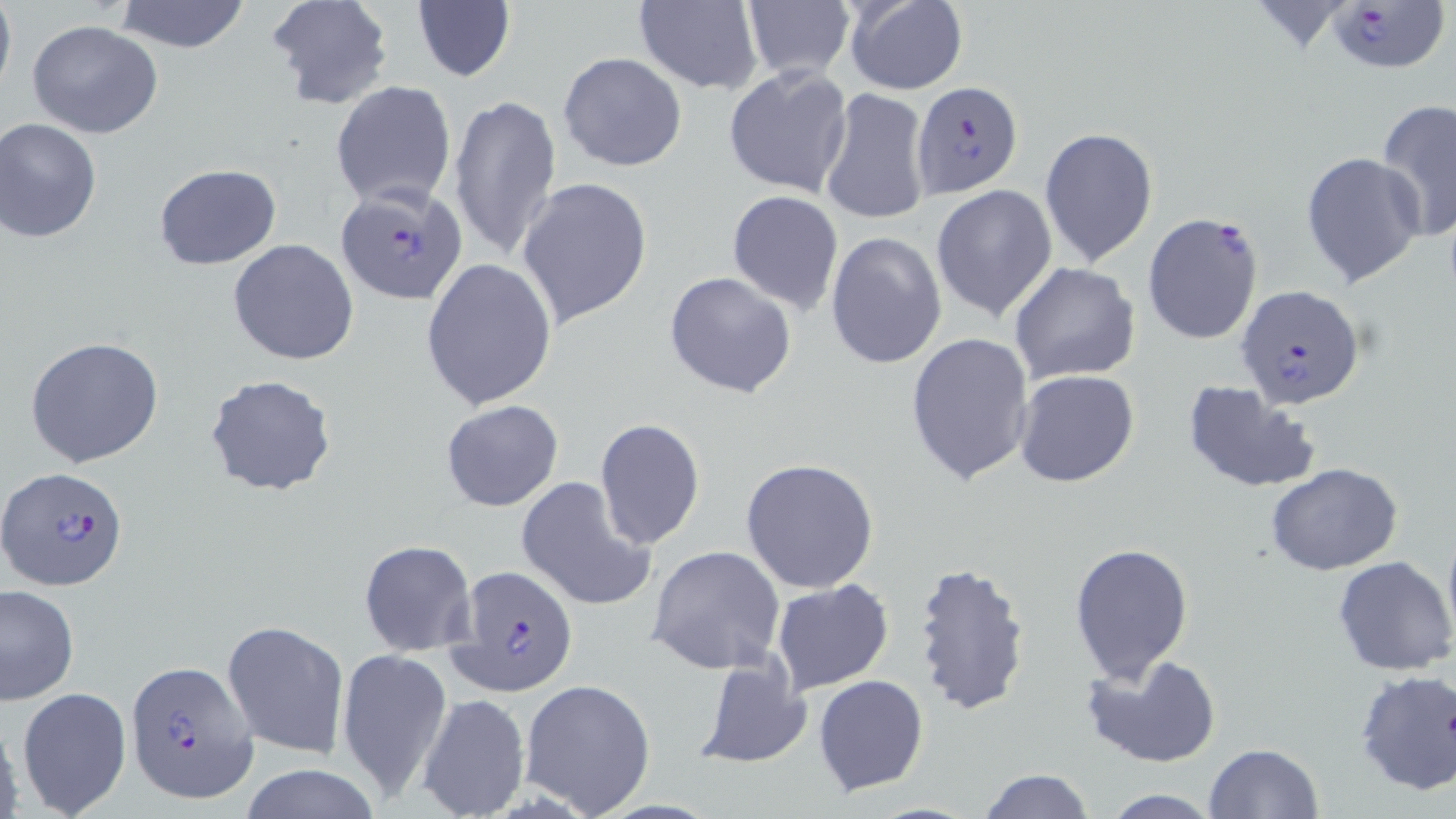
Summary:
  - Coordinate format: approximate bounding boxes as (x1,y1)-(x2,y2) corner pairs in pixels
  - Uninfected red blood cell locations: (0,0)-(16,100), (112,0)-(253,53), (266,0)-(394,112), (631,0)-(764,95), (842,0)-(969,95), (741,1)-(855,83), (410,3)-(517,85), (26,21)-(165,138), (557,51)-(688,173), (722,65)-(853,199), (331,80)-(457,210), (819,88)-(930,227), (448,93)-(562,264), (1375,99)-(1456,241), (1,118)-(103,242), (1039,127)-(1159,267), (1300,152)-(1425,290), (153,164)-(282,270), (516,176)-(653,330), (930,184)-(1057,322), (727,190)-(845,314), (825,231)-(946,371), (228,238)-(357,364), (420,257)-(558,410), (1009,263)-(1141,386), (663,270)-(798,400), (905,332)-(1036,486), (24,336)-(167,468), (1013,369)-(1141,489), (205,374)-(338,499), (1182,381)-(1320,493), (440,399)-(564,512), (594,419)-(706,549), (740,457)-(879,594), (1266,463)-(1404,576), (516,476)-(658,614), (1442,518)-(1456,649), (358,539)-(477,656), (1069,541)-(1195,685), (645,545)-(784,674), (1333,556)-(1455,675), (910,561)-(1032,717), (771,579)-(894,696), (2,584)-(78,705), (785,608)-(912,751), (221,620)-(349,757), (337,647)-(451,805), (693,654)-(813,770), (1081,654)-(1223,768), (1353,667)-(1456,796), (812,674)-(929,796), (519,678)-(657,817), (16,685)-(134,818), (415,693)-(530,819), (0,712)-(25,817), (1205,743)-(1324,818), (238,762)-(383,819), (977,767)-(1094,818), (1098,791)-(1224,819)
  - Plasmodium falciparum-infected red blood cell locations: (1325,1)-(1448,71), (909,81)-(1020,200), (335,183)-(470,307), (1141,212)-(1264,344), (1235,285)-(1365,411), (2,468)-(129,590), (448,564)-(578,694), (126,662)-(258,803)
  - Slide-level diagnosis: Plasmodium falciparum
  - Preparation: thin blood film
  - Stain: May-Grünwald-Giemsa
  - Modality: optical microscopy
  - Magnification: 1000x
  - Image size: 1456×819 pixels
  - Field of view: single